Comment on the morphology of the red blood cells.
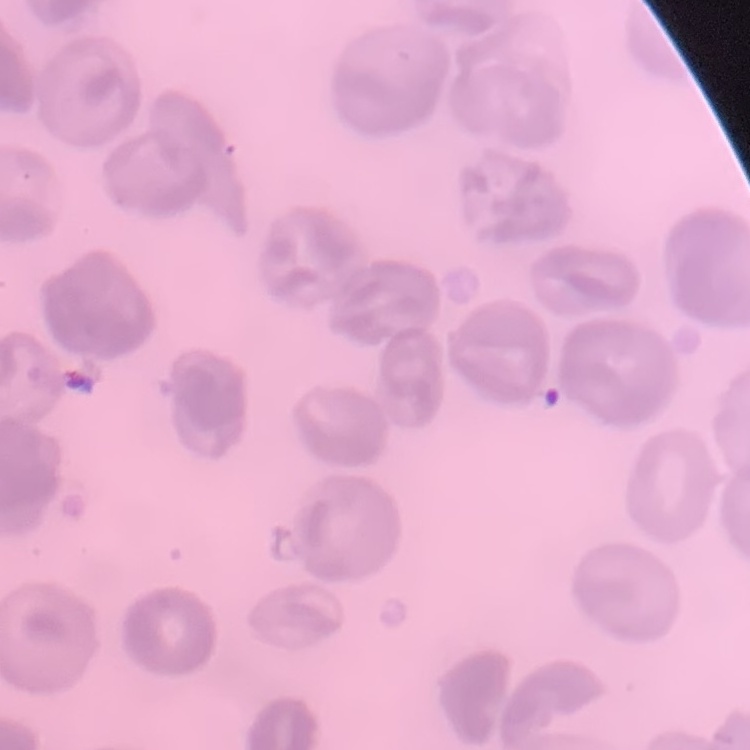
They show no rouleaux formation.

stain: Field's or Giemsa
preparation: thin blood film
image_type: one tile cut from a larger photomicrograph